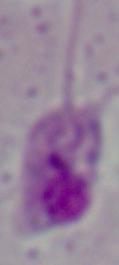

Summary:
  - Identification: Leishmania
  - Magnification: 1000x
  - Modality: micrograph